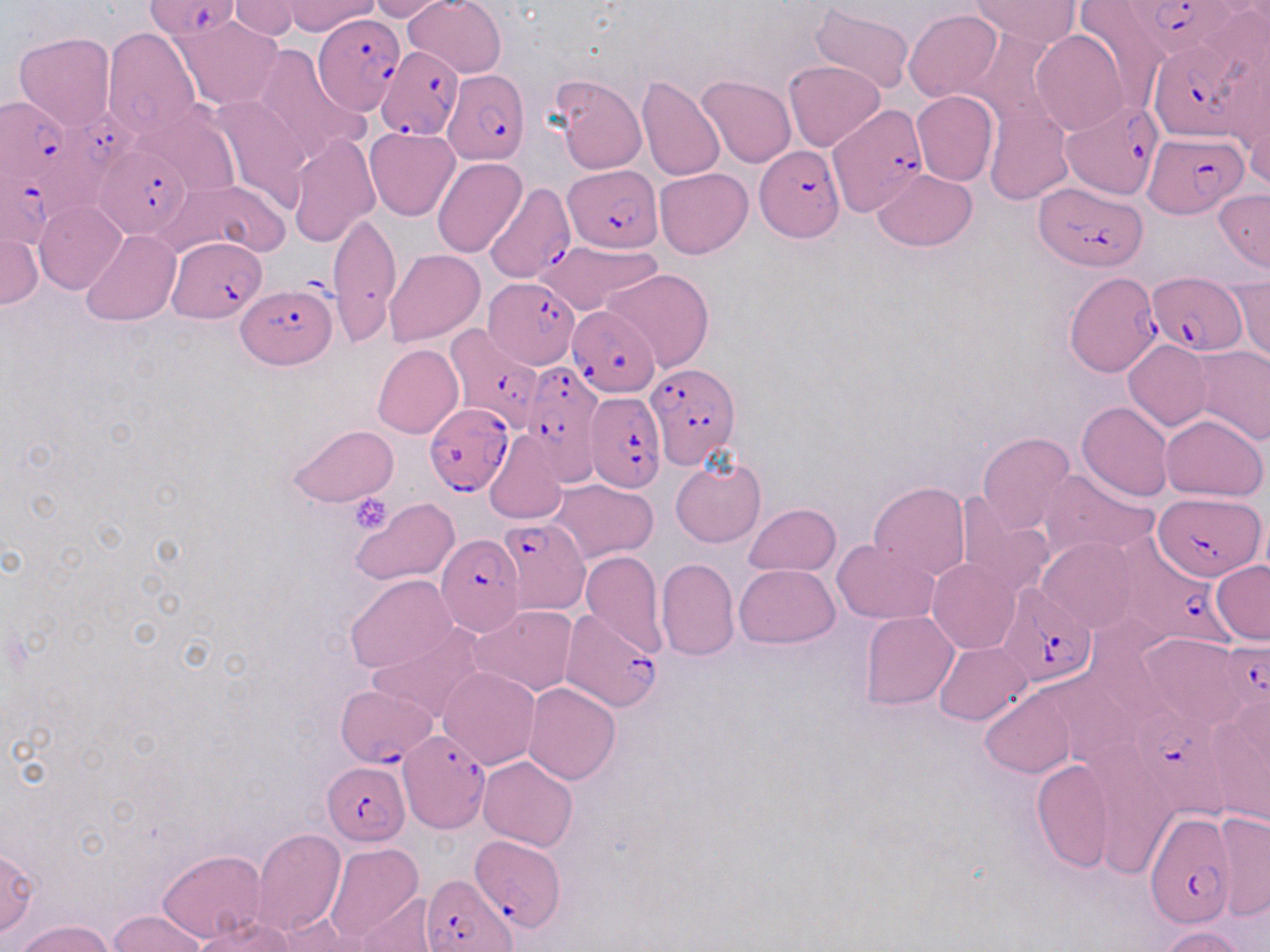 Approximate bounding boxes as (x1,y1)-(x2,y2) corner pairs in pixels. Uninfected red blood cell locations: (229,0)-(305,39), (368,0)-(450,21), (403,0)-(506,77), (970,0)-(1080,47), (270,1)-(382,37), (1074,1)-(1169,107), (810,4)-(916,95), (904,9)-(1001,102), (169,17)-(283,109), (966,26)-(1064,132), (104,28)-(201,137), (1030,29)-(1128,135), (13,31)-(116,131), (251,44)-(369,166), (784,60)-(885,151), (637,74)-(725,180), (549,75)-(647,175), (697,76)-(797,168), (1241,90)-(1269,195), (912,91)-(999,186), (205,95)-(313,215), (141,101)-(243,198), (985,103)-(1071,205), (365,127)-(459,220), (289,133)-(380,247), (433,158)-(526,259), (655,168)-(753,258), (872,169)-(977,251), (162,180)-(291,260), (1214,188)-(1270,272), (36,202)-(127,295), (328,212)-(402,343), (0,229)-(41,311), (82,230)-(180,327), (538,239)-(662,316), (385,248)-(486,346), (603,268)-(715,373), (1227,274)-(1269,362), (1123,339)-(1213,430), (372,344)-(462,438), (1193,345)-(1270,444), (1077,401)-(1172,500), (1160,414)-(1268,499), (287,424)-(397,507), (484,430)-(569,524), (977,432)-(1075,532), (671,458)-(766,548), (1040,468)-(1160,561), (549,479)-(658,563), (868,483)-(969,581), (955,494)-(1054,599), (350,498)-(459,585), (744,502)-(841,576), (1038,537)-(1141,632), (831,539)-(939,624), (581,551)-(667,657), (655,558)-(740,660), (927,558)-(1019,654), (1212,560)-(1270,643), (734,564)-(840,647), (345,575)-(457,672), (471,605)-(578,697), (860,612)-(957,710), (367,624)-(486,724), (1135,632)-(1250,729), (934,641)-(1031,726), (437,667)-(540,769), (523,682)-(620,784), (981,687)-(1076,778), (1206,702)-(1270,825), (478,756)-(578,850), (1091,756)-(1179,880), (1031,758)-(1115,872), (1212,811)-(1269,920), (251,829)-(345,936), (325,842)-(423,942), (0,847)-(40,937), (157,850)-(267,943), (358,892)-(439,952), (106,909)-(208,952), (194,914)-(295,951), (279,914)-(374,950), (15,919)-(117,952), (1159,925)-(1249,952). Plasmodium falciparum-infected red blood cell locations: (148,0)-(240,42), (1120,2)-(1244,63), (313,13)-(406,115), (1147,35)-(1261,143), (377,47)-(463,140), (442,70)-(529,164), (1062,100)-(1164,201), (0,101)-(72,183), (817,107)-(929,221), (34,111)-(142,218), (1144,129)-(1241,217), (95,144)-(192,238), (756,147)-(843,243), (0,164)-(64,249), (564,166)-(661,252), (486,182)-(580,290), (1033,184)-(1148,272), (167,235)-(268,322), (1146,270)-(1243,354), (1065,271)-(1162,377), (484,276)-(581,369), (236,282)-(337,370), (568,305)-(660,395), (441,324)-(544,432), (516,363)-(601,480), (646,363)-(739,467), (586,390)-(665,492), (423,403)-(515,496), (1154,493)-(1266,581), (500,516)-(591,614), (435,531)-(524,639), (1120,531)-(1250,655), (995,582)-(1098,687), (561,610)-(661,710), (1219,642)-(1270,713), (337,686)-(435,764), (1130,702)-(1213,788), (396,723)-(492,832), (323,762)-(409,846), (1145,812)-(1238,930), (470,832)-(565,931), (422,874)-(518,952). Platelet locations: (349,493)-(392,533). Slide-level diagnosis: Plasmodium falciparum. Optical microscopy. Thin blood film. May-Grünwald-Giemsa-stained preparation. One field of a larger specimen. 1000x magnification. Image is 1270×952 pixels.